State which cell type is depicted.
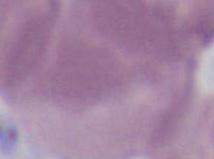
This is an erythrocyte.

modality = micrograph
magnification = 1000x